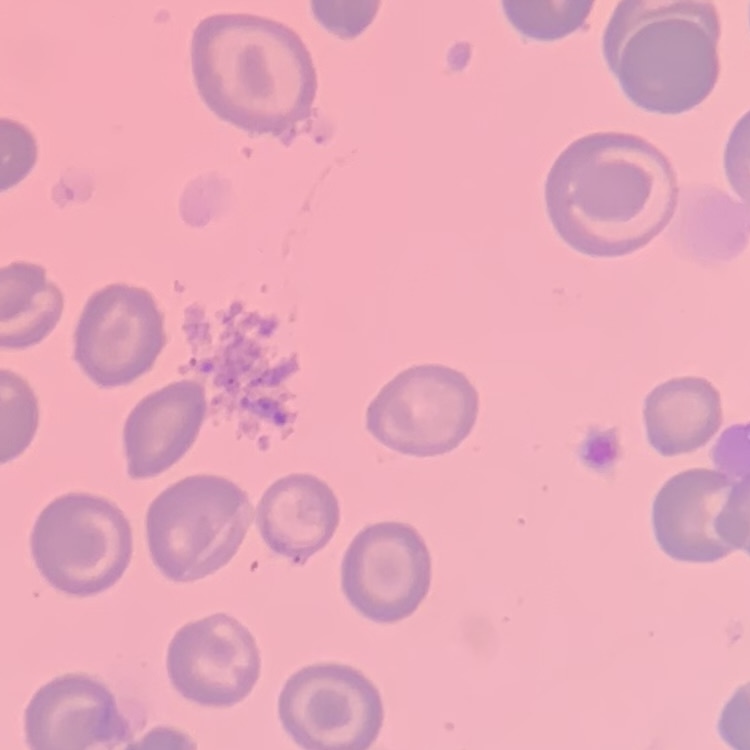
Summary:
  - Erythrocyte morphology: no rouleaux formation
  - Preparation: thin blood film
  - Stain: Field's or Giemsa
  - Image type: one tile cut from a larger photomicrograph